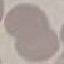 Malaria status: uninfected. Thin blood smear. Acquired by smartphone through the microscope eyepiece. Giemsa stain. Automatically extracted cell patch, resized to 64 × 64 pixels.